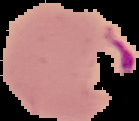

Malaria status: parasitized. From a thin blood smear. Image is 139×121 pixels. The area outside the segmented cell region is set to black.